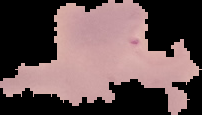
{
  "image_type": "segmented cell region with the area outside set to black",
  "result": "malaria parasites detected",
  "preparation": "thin blood smear",
  "image_size": "202×115 pixels"
}